Locate every blood parasite and identify its species.
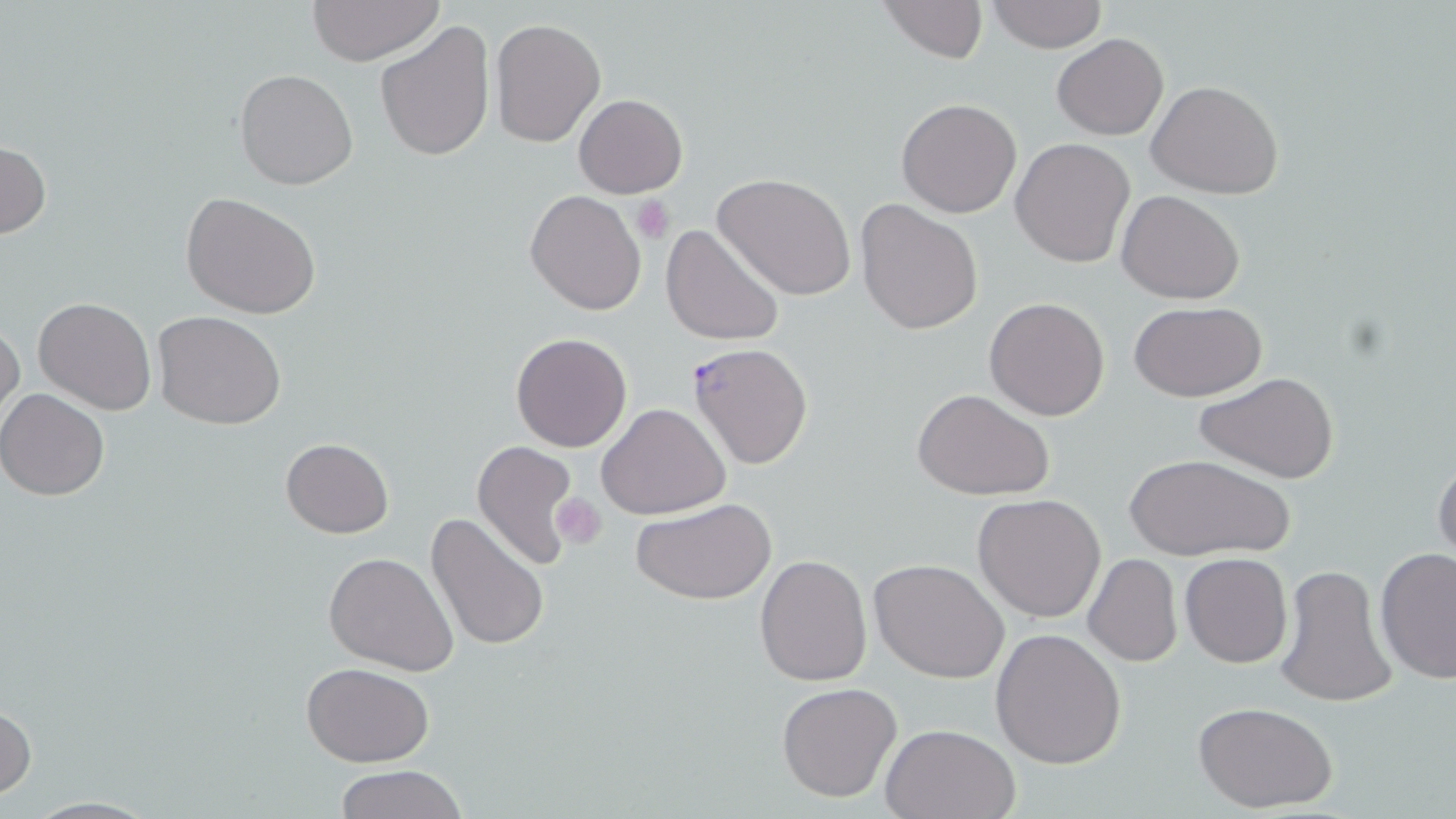

Approximate bounding boxes as (x1,y1)-(x2,y2) corner pairs in pixels.
Plasmodium falciparum-infected red blood cells: (689,343)-(814,469).
No Plasmodium ovale, Plasmodium malariae, Plasmodium vivax, Babesia divergens, or Trypanosoma brucei observed.

slide-level diagnosis = Plasmodium falciparum
field of view = one of a larger specimen
stain = May-Grünwald-Giemsa
modality = optical microscopy
uninfected red blood cell locations = approximate bounding boxes as (x1,y1)-(x2,y2) corner pairs in pixels: (878,0)-(989,64), (988,0)-(1107,52), (306,1)-(446,67), (489,17)-(605,147), (374,20)-(494,162), (1052,32)-(1168,140), (233,68)-(359,191), (1147,80)-(1283,198), (574,93)-(686,197), (896,98)-(1022,219), (1011,137)-(1135,268), (0,141)-(51,240), (714,173)-(857,300), (526,189)-(647,315), (1117,190)-(1245,305), (180,191)-(323,320), (855,199)-(984,336), (661,223)-(784,347), (33,296)-(157,415), (985,297)-(1110,420), (1128,299)-(1267,402), (153,310)-(286,430), (0,318)-(24,430), (511,331)-(633,452), (1194,371)-(1341,485), (913,387)-(1055,500), (0,389)-(109,500), (597,402)-(731,519), (281,437)-(394,538), (470,440)-(579,572), (1126,453)-(1295,563), (1432,457)-(1456,568), (972,493)-(1105,622), (631,498)-(778,606), (425,512)-(548,653), (1374,548)-(1456,684), (323,552)-(458,676), (1180,552)-(1292,668), (755,554)-(871,686), (1085,554)-(1182,667), (869,558)-(1010,684), (1275,565)-(1394,707), (1036,567)-(1157,720), (990,626)-(1126,769), (301,662)-(435,767), (776,681)-(903,803), (0,701)-(36,800), (1192,701)-(1339,814), (881,723)-(1023,819), (332,767)-(470,819), (13,795)-(167,818)
preparation = thin blood smear
platelet locations = approximate bounding boxes as (x1,y1)-(x2,y2) corner pairs in pixels: (631,194)-(676,243), (551,493)-(607,548)
image size = 1456×819 pixels
magnification = 1000x